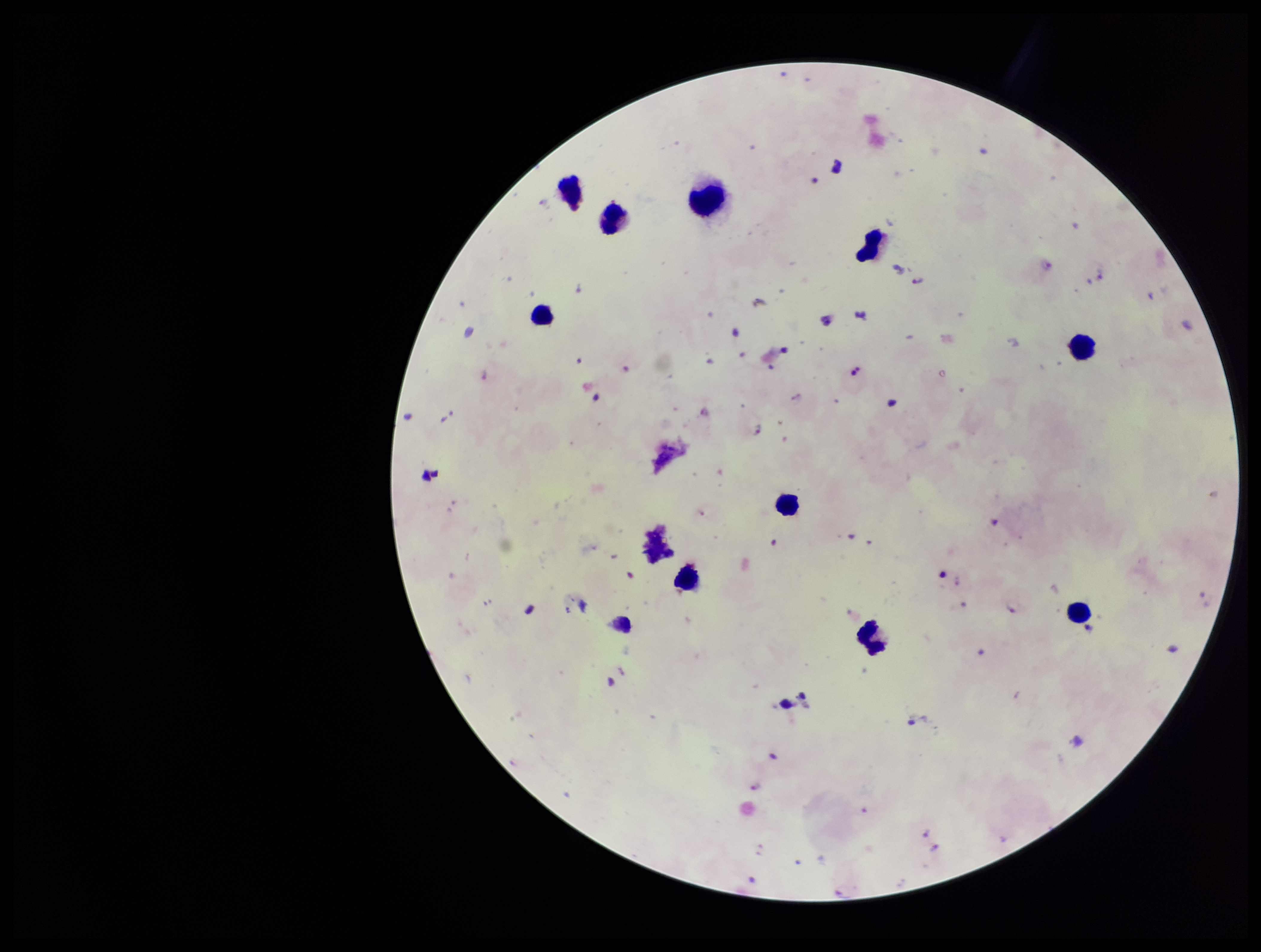
stain: Giemsa
image_size: 1261×952 pixels
field_of_view: single
species_reported_for_this_patient: Plasmodium falciparum
leukocyte_count: 11
plasmodium_parasites: detected
parasite_count: 13
capture: smartphone photograph through the microscope eyepiece
preparation: thick
patient_malaria_status: infected